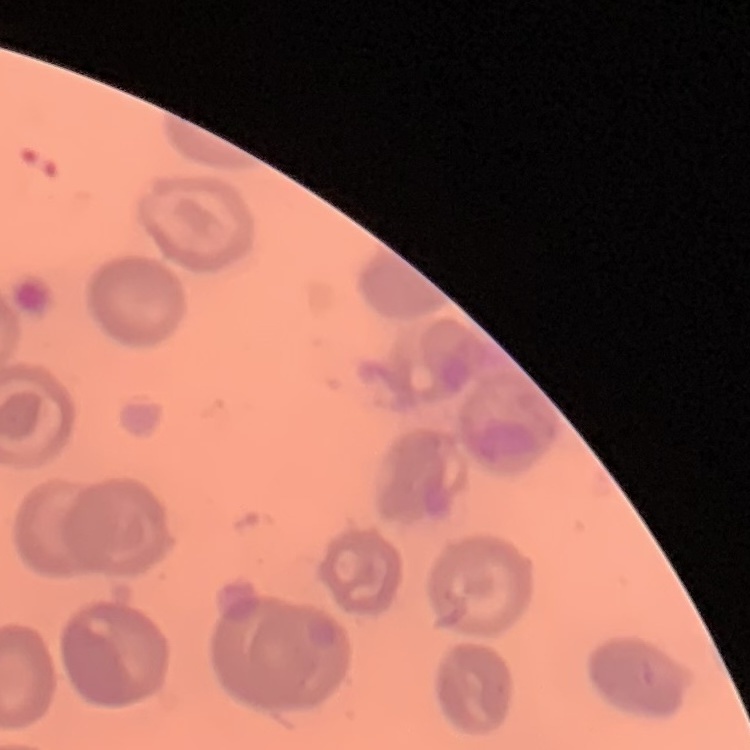

The erythrocytes exhibit no rouleaux formation. One tile cut from a larger photomicrograph. Field's or Giemsa stain. Thin peripheral smear.